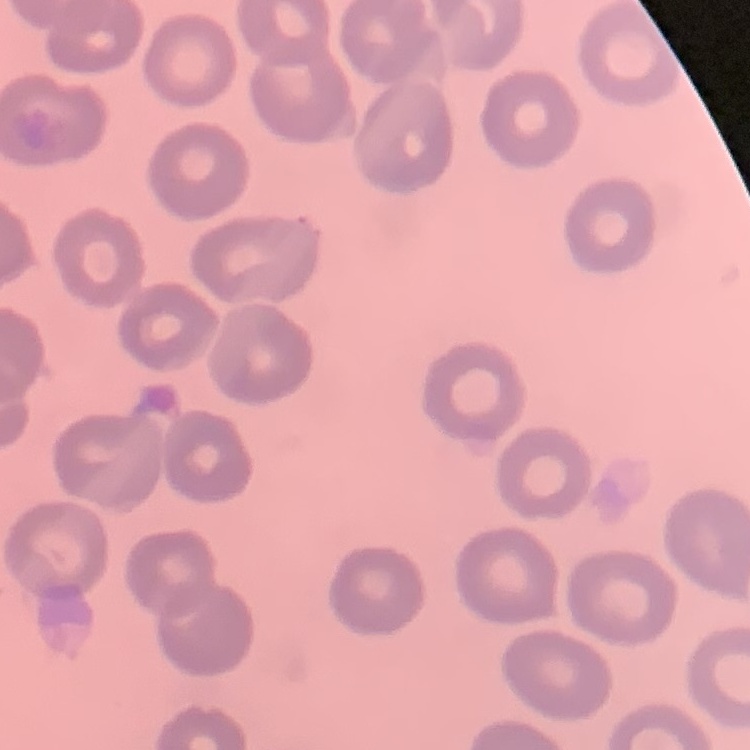
The red blood cells exhibit no rouleaux formation. Stained with either Field's or Giemsa. Square crop of a larger photomicrograph. Thin blood film.